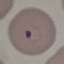
Result: malaria parasites identified. Thin blood film. Acquired by smartphone through the microscope eyepiece. Automatically extracted cell patch, resized to 64 × 64 pixels. Giemsa-stained preparation.